State which parasite is depicted.
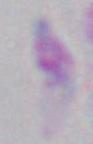

Toxoplasma gondii.

modality = photomicrograph
magnification = 1000x